Point out each malaria parasite and each leukocyte.
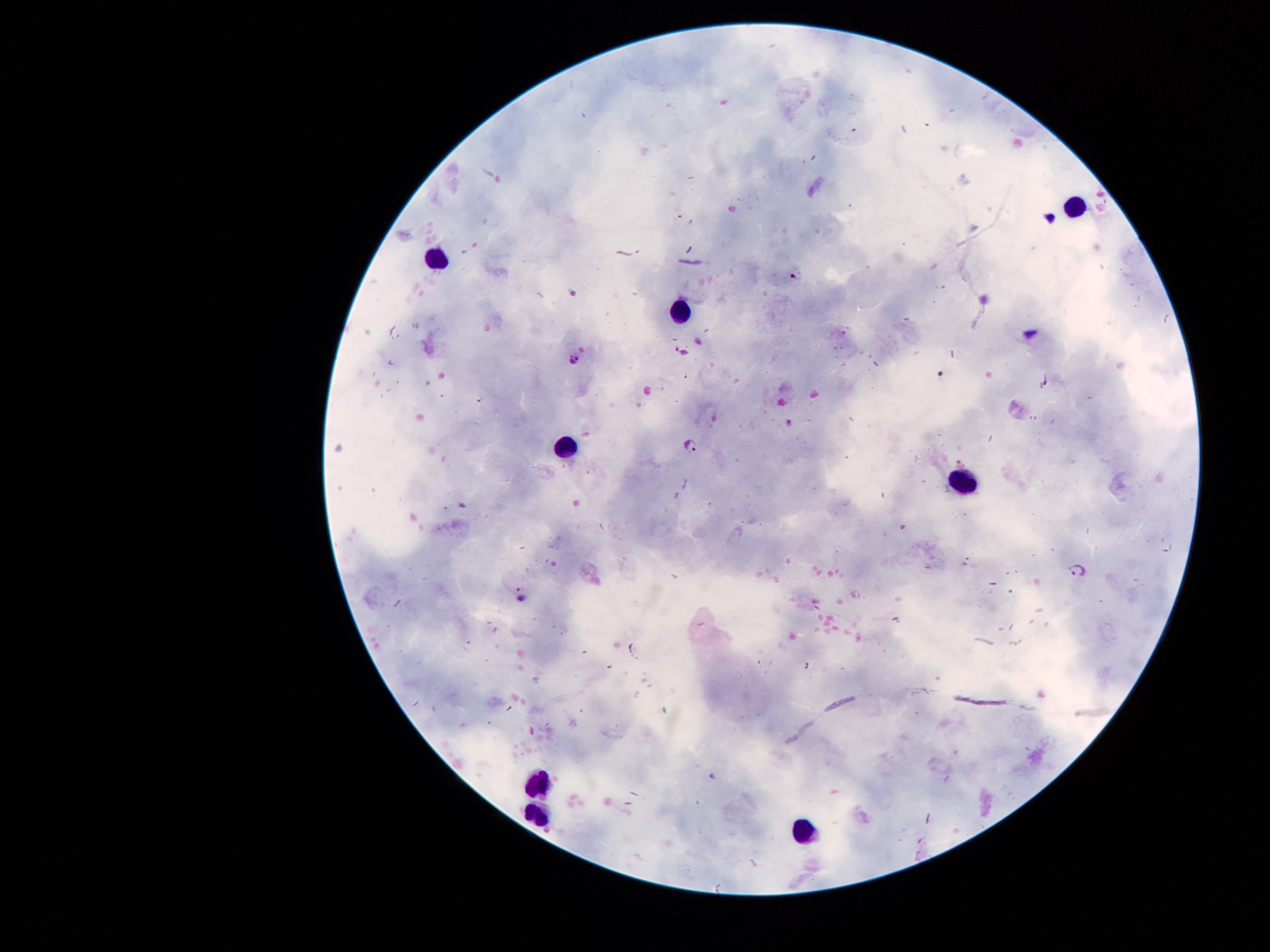
Approximate centers as (x, y) in pixels.
Malaria parasites: (573, 362), (690, 445), (1079, 571).
Leukocytes: (1071, 206), (434, 261), (680, 309), (567, 446), (954, 484), (544, 784), (534, 806), (806, 829).

magnification = 100x
field of view = single
stain = Giemsa
preparation = thick blood film
patient malaria status = infected with Plasmodium falciparum
image size = 1270×952 pixels
capture = smartphone through the microscope eyepiece